Locate every blood parasite and identify its species.
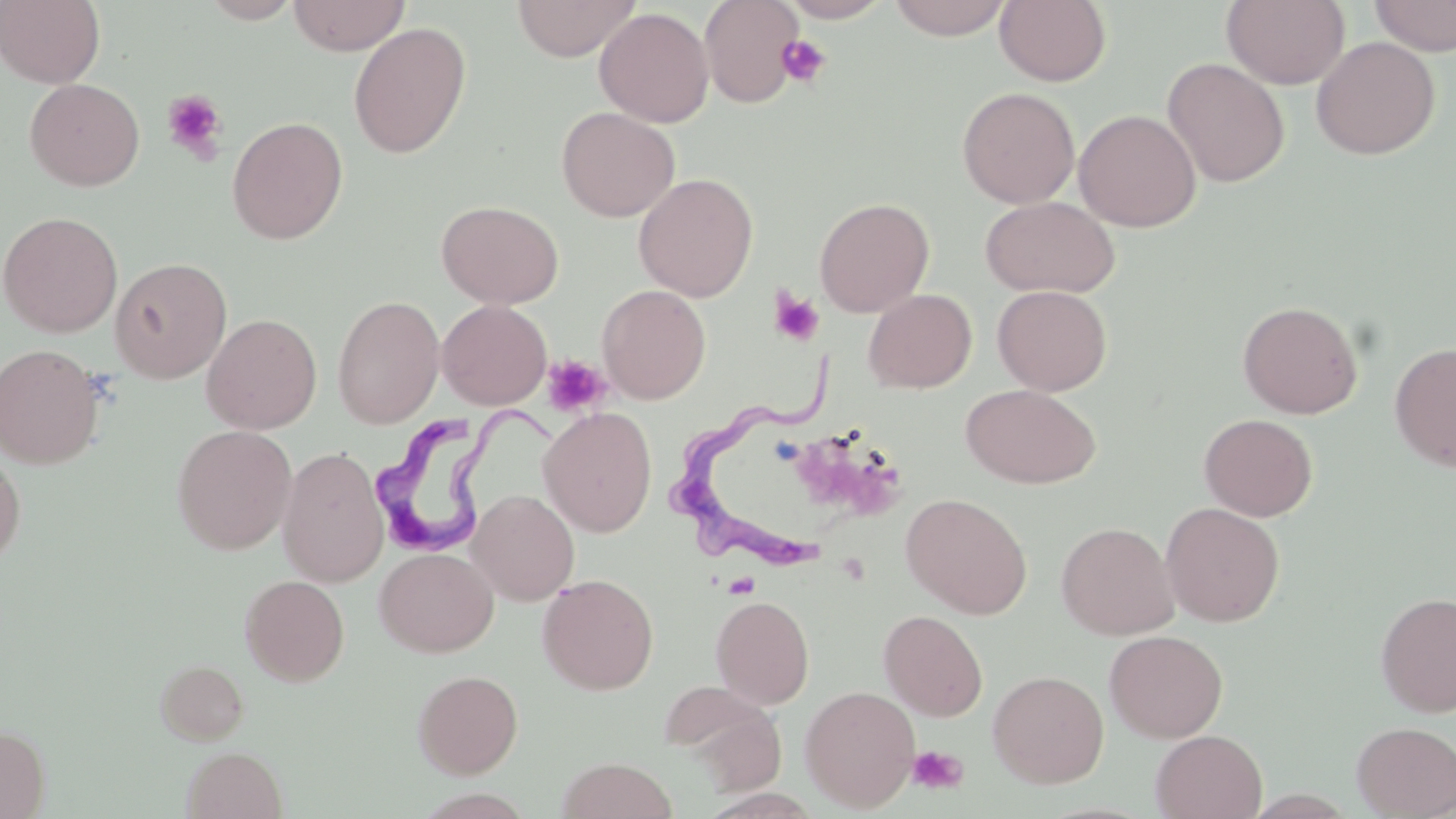

Approximate bounding boxes as named x1/y1/x2/y2 corners in pixels.
Trypanosoma brucei: (x1=672, y1=354, x2=833, y2=573), (x1=373, y1=400, x2=563, y2=553).
No Plasmodium falciparum, Plasmodium ovale, Plasmodium malariae, Plasmodium vivax, or Babesia divergens observed.

slide-level diagnosis = Trypanosoma brucei
image size = 1456×819 pixels
magnification = 1000x
platelet locations = approximate bounding boxes as named x1/y1/x2/y2 corners in pixels: (x1=776, y1=36, x2=831, y2=88), (x1=161, y1=90, x2=228, y2=163), (x1=768, y1=287, x2=824, y2=347), (x1=544, y1=354, x2=614, y2=417), (x1=802, y1=438, x2=905, y2=511), (x1=907, y1=745, x2=968, y2=794)
stain = May-Grünwald-Giemsa
modality = light microscopy
field of view = single
preparation = thin blood film
uninfected red blood cell locations = approximate bounding boxes as named x1/y1/x2/y2 corners in pixels: (x1=0, y1=0, x2=106, y2=88), (x1=199, y1=0, x2=303, y2=23), (x1=288, y1=0, x2=410, y2=55), (x1=512, y1=0, x2=641, y2=60), (x1=699, y1=0, x2=805, y2=108), (x1=781, y1=0, x2=892, y2=22), (x1=887, y1=0, x2=1013, y2=41), (x1=994, y1=0, x2=1111, y2=86), (x1=1221, y1=0, x2=1350, y2=89), (x1=1368, y1=0, x2=1456, y2=56), (x1=594, y1=7, x2=714, y2=127), (x1=348, y1=23, x2=471, y2=158), (x1=1311, y1=36, x2=1441, y2=160), (x1=1162, y1=57, x2=1290, y2=187), (x1=24, y1=78, x2=145, y2=191), (x1=957, y1=86, x2=1080, y2=208), (x1=556, y1=106, x2=680, y2=222), (x1=1073, y1=109, x2=1201, y2=232), (x1=226, y1=115, x2=349, y2=245), (x1=633, y1=172, x2=759, y2=302), (x1=979, y1=195, x2=1120, y2=298), (x1=814, y1=196, x2=934, y2=317), (x1=436, y1=199, x2=564, y2=308), (x1=1, y1=211, x2=123, y2=338), (x1=110, y1=257, x2=232, y2=383), (x1=597, y1=284, x2=711, y2=404), (x1=992, y1=285, x2=1112, y2=395), (x1=863, y1=289, x2=977, y2=393), (x1=332, y1=294, x2=445, y2=428), (x1=437, y1=299, x2=552, y2=410), (x1=1237, y1=300, x2=1363, y2=418), (x1=202, y1=313, x2=322, y2=434), (x1=1389, y1=342, x2=1456, y2=472), (x1=1, y1=343, x2=106, y2=469), (x1=960, y1=383, x2=1101, y2=489), (x1=538, y1=407, x2=657, y2=537), (x1=1199, y1=413, x2=1318, y2=521), (x1=172, y1=424, x2=297, y2=555), (x1=277, y1=446, x2=388, y2=587), (x1=0, y1=449, x2=25, y2=571), (x1=467, y1=489, x2=579, y2=605), (x1=901, y1=493, x2=1033, y2=618), (x1=1160, y1=502, x2=1285, y2=627), (x1=1056, y1=521, x2=1179, y2=639), (x1=374, y1=547, x2=498, y2=657), (x1=537, y1=573, x2=659, y2=694), (x1=240, y1=574, x2=349, y2=686), (x1=1375, y1=591, x2=1456, y2=718), (x1=711, y1=595, x2=814, y2=709), (x1=879, y1=609, x2=988, y2=721), (x1=1104, y1=629, x2=1228, y2=743), (x1=154, y1=658, x2=249, y2=745), (x1=412, y1=669, x2=523, y2=778), (x1=987, y1=670, x2=1109, y2=789), (x1=662, y1=682, x2=785, y2=786), (x1=800, y1=684, x2=920, y2=812), (x1=1352, y1=721, x2=1456, y2=818), (x1=0, y1=724, x2=50, y2=819), (x1=1150, y1=730, x2=1267, y2=818), (x1=181, y1=747, x2=287, y2=819), (x1=556, y1=757, x2=678, y2=819)